Classify this cell by malaria status.
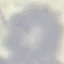

It is uninfected.

{
  "stain": "Giemsa",
  "image_type": "cell patch, automatically extracted from a larger field of view and resized to 64 × 64 pixels",
  "preparation": "thin blood smear",
  "capture": "smartphone camera at the microscope eyepiece"
}